Outline platelets.
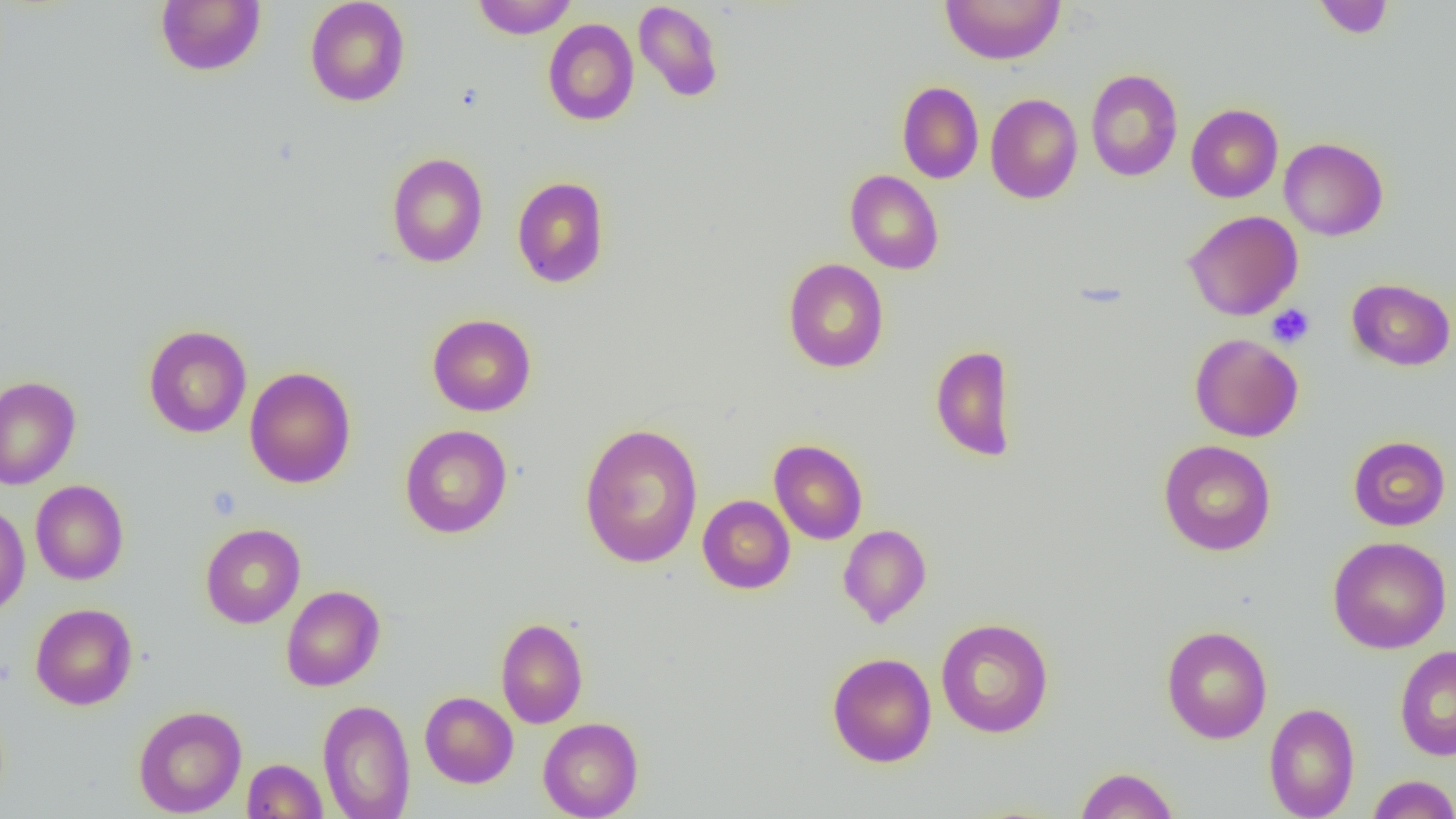
Approximate bounding boxes as (x1,y1)-(x2,y2) corner pairs in pixels.
Platelets: (1266,304)-(1315,349).

slide-level diagnosis = no evidence of blood parasites
magnification = 1000x
image size = 1456×819 pixels
uninfected red blood cell locations = approximate bounding boxes as (x1,y1)-(x2,y2) corner pairs in pixels: (155,0)-(266,76), (305,0)-(410,107), (471,0)-(577,39), (940,0)-(1065,65), (1312,0)-(1395,39), (633,1)-(724,102), (543,18)-(639,126), (1085,68)-(1183,182), (896,81)-(984,183), (985,93)-(1083,204), (1186,104)-(1283,203), (1279,138)-(1388,240), (386,152)-(488,267), (845,170)-(944,275), (512,176)-(610,288), (1184,210)-(1303,321), (783,258)-(889,373), (1347,278)-(1455,371), (427,313)-(536,416), (143,324)-(252,438), (1189,333)-(1303,442), (929,344)-(1018,462), (244,366)-(356,488), (0,376)-(81,489), (579,422)-(704,569), (400,424)-(512,538), (1348,435)-(1451,531), (769,439)-(868,545), (1158,439)-(1276,556), (30,480)-(129,585), (698,494)-(795,594), (0,503)-(30,617), (201,523)-(305,628), (838,524)-(931,627), (1327,536)-(1451,653), (281,585)-(385,691), (30,602)-(137,710), (936,617)-(1054,737), (495,618)-(588,728), (1161,625)-(1272,744), (1394,645)-(1456,761), (827,652)-(937,767), (420,691)-(518,788), (317,699)-(416,819), (1263,702)-(1360,819), (133,705)-(247,817), (538,717)-(644,818), (242,758)-(328,819), (1074,766)-(1180,818), (1367,774)-(1456,819)
preparation = thin blood film
field of view = one of a larger specimen
modality = light microscopy